Classify this cell by malaria status.
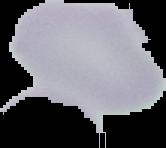
Uninfected.

Summary:
  - Preparation: thin blood film
  - Image type: cell region segmented out of the field of view; surrounding area masked to black
  - Image size: 166×148 pixels